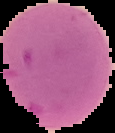

Segmented cell region on a black background. From a thin blood film. Result: no malaria parasites seen. Image is 115×133 pixels.